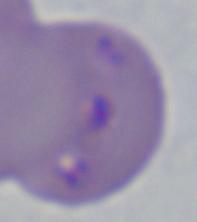
modality = photomicrograph
identification = Babesia
magnification = 1000x